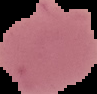
Summary:
  - Image type: cell region segmented out of the field of view; surrounding area masked to black
  - Preparation: thin blood smear
  - Image size: 97×94 pixels
  - Malaria status: uninfected